Locate every malaria parasite.
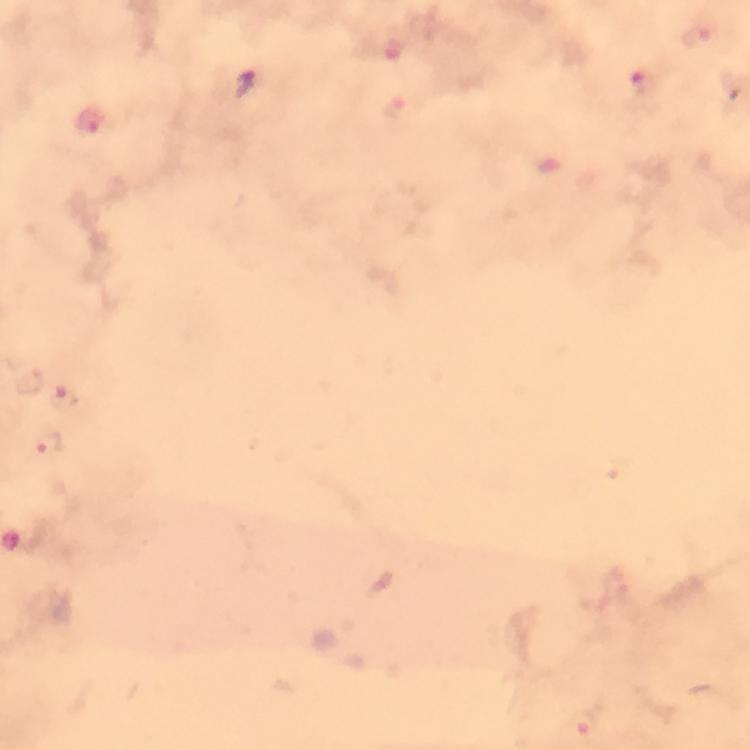
Approximate centers as (x, y) in pixels.
Malaria parasites: (702, 35), (646, 84), (396, 110), (92, 121), (30, 381), (50, 443), (582, 724).

Immersion oil was used. Cropped region of a single field of view. Giemsa stain. Photographed through the microscope with a smartphone camera. From a diagnostic examination for malaria. Thick blood film. 100x magnification. Image is 750×750 pixels.